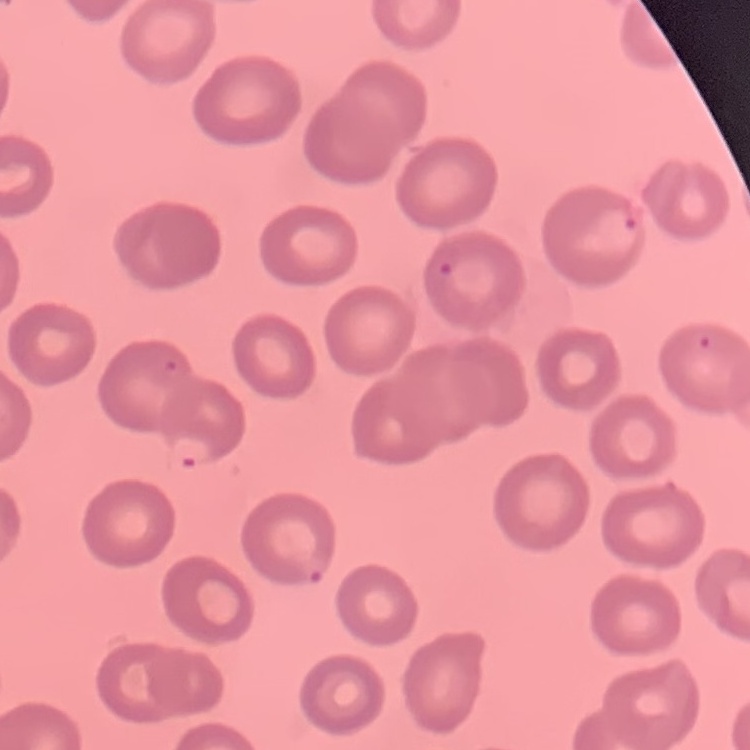
Summary:
  - Red blood cell morphology: no rouleaux formation
  - Preparation: thin peripheral smear
  - Image type: one tile cut from a larger photomicrograph
  - Stain: Field's or Giemsa